Comment on the morphology of the red blood cells.
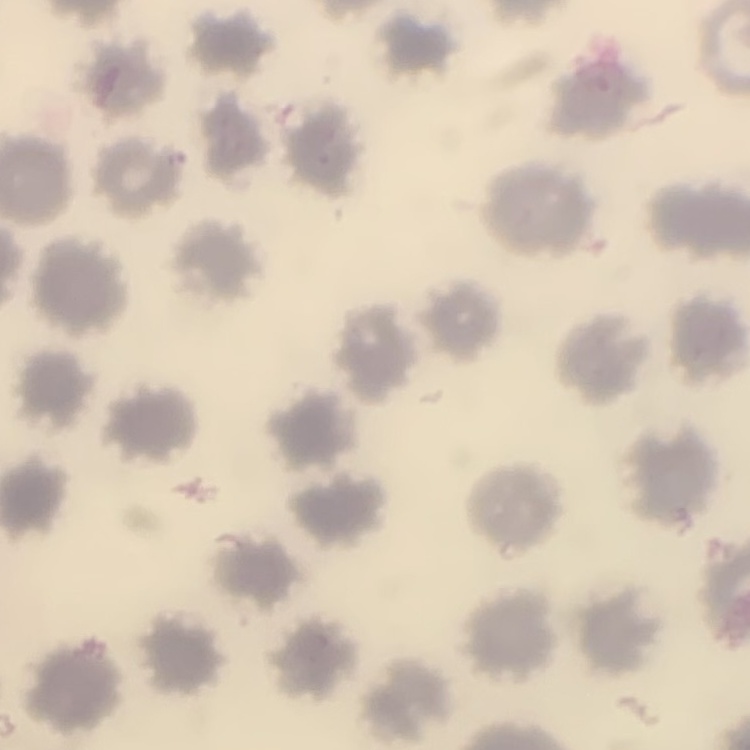

No rouleaux formation.

Square crop of a larger photomicrograph. Thin peripheral smear. Stained with either Field's or Giemsa.